Locate every malaria parasite and every leukocyte.
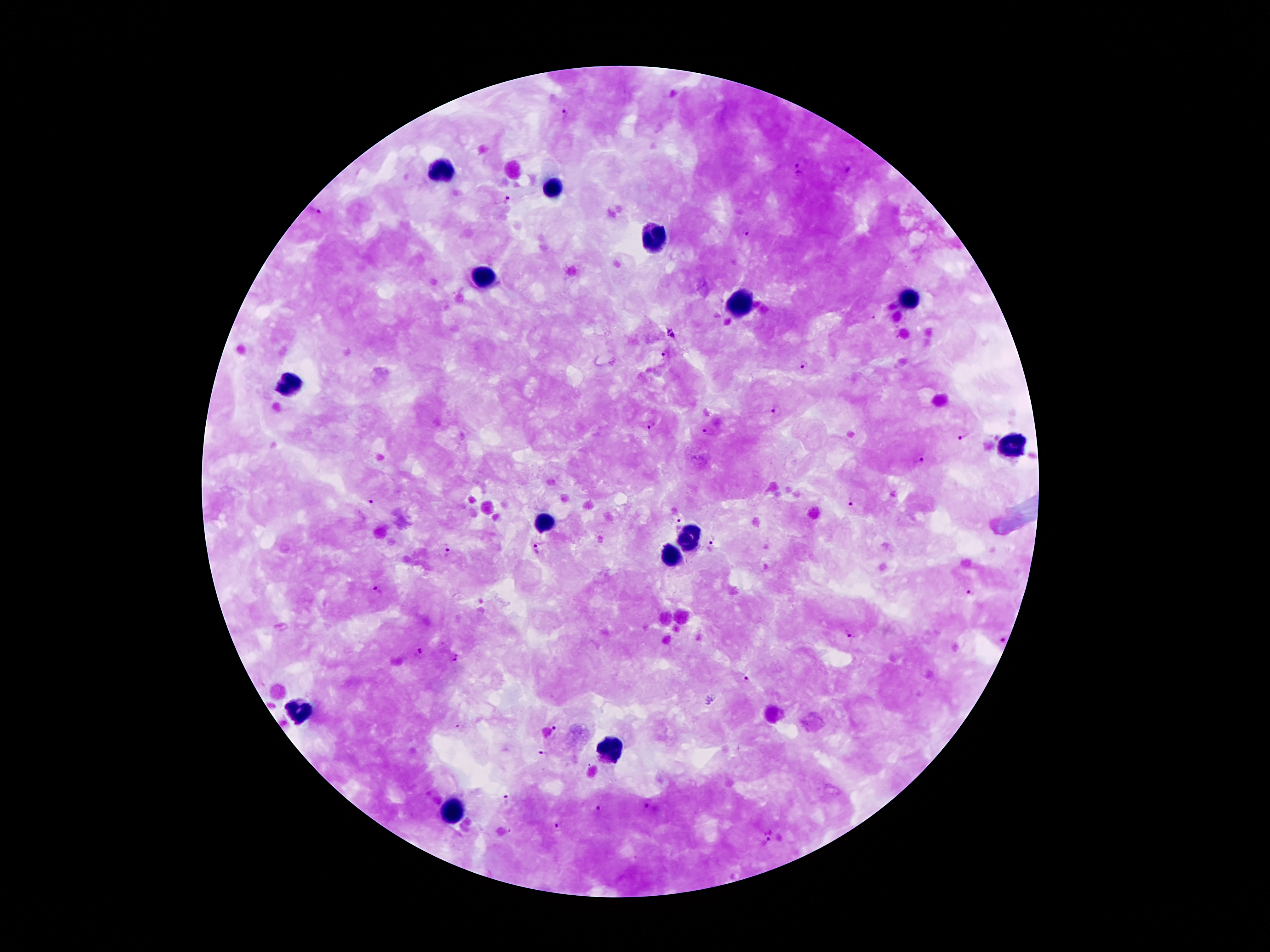
Approximate object centers, in pixels from the top-left corner.
Malaria parasites: (x=563, y=114), (x=798, y=164), (x=799, y=174), (x=507, y=200), (x=313, y=211), (x=748, y=234), (x=871, y=318), (x=673, y=336), (x=664, y=355), (x=807, y=365), (x=776, y=411), (x=650, y=426), (x=710, y=431), (x=966, y=436), (x=918, y=457), (x=373, y=500), (x=852, y=503), (x=676, y=524), (x=714, y=541), (x=538, y=546), (x=446, y=548), (x=378, y=588), (x=970, y=591), (x=852, y=632), (x=1001, y=638), (x=420, y=653), (x=455, y=660), (x=746, y=679), (x=461, y=726), (x=556, y=728), (x=545, y=753), (x=509, y=796), (x=645, y=806), (x=597, y=809), (x=554, y=827), (x=511, y=831), (x=768, y=835).
Leukocytes: (x=444, y=169), (x=550, y=186), (x=649, y=238), (x=481, y=280), (x=911, y=302), (x=738, y=306), (x=288, y=384), (x=1015, y=445), (x=548, y=522), (x=691, y=537), (x=671, y=556), (x=301, y=710), (x=610, y=752), (x=454, y=810).

Summary:
  - Field of view: one from this slide
  - Capture: smartphone through the microscope eyepiece
  - Stain: Giemsa
  - Magnification: 100x
  - Preparation: thick blood smear
  - Patient malaria status: positive for Plasmodium falciparum
  - Image size: 1270×952 pixels